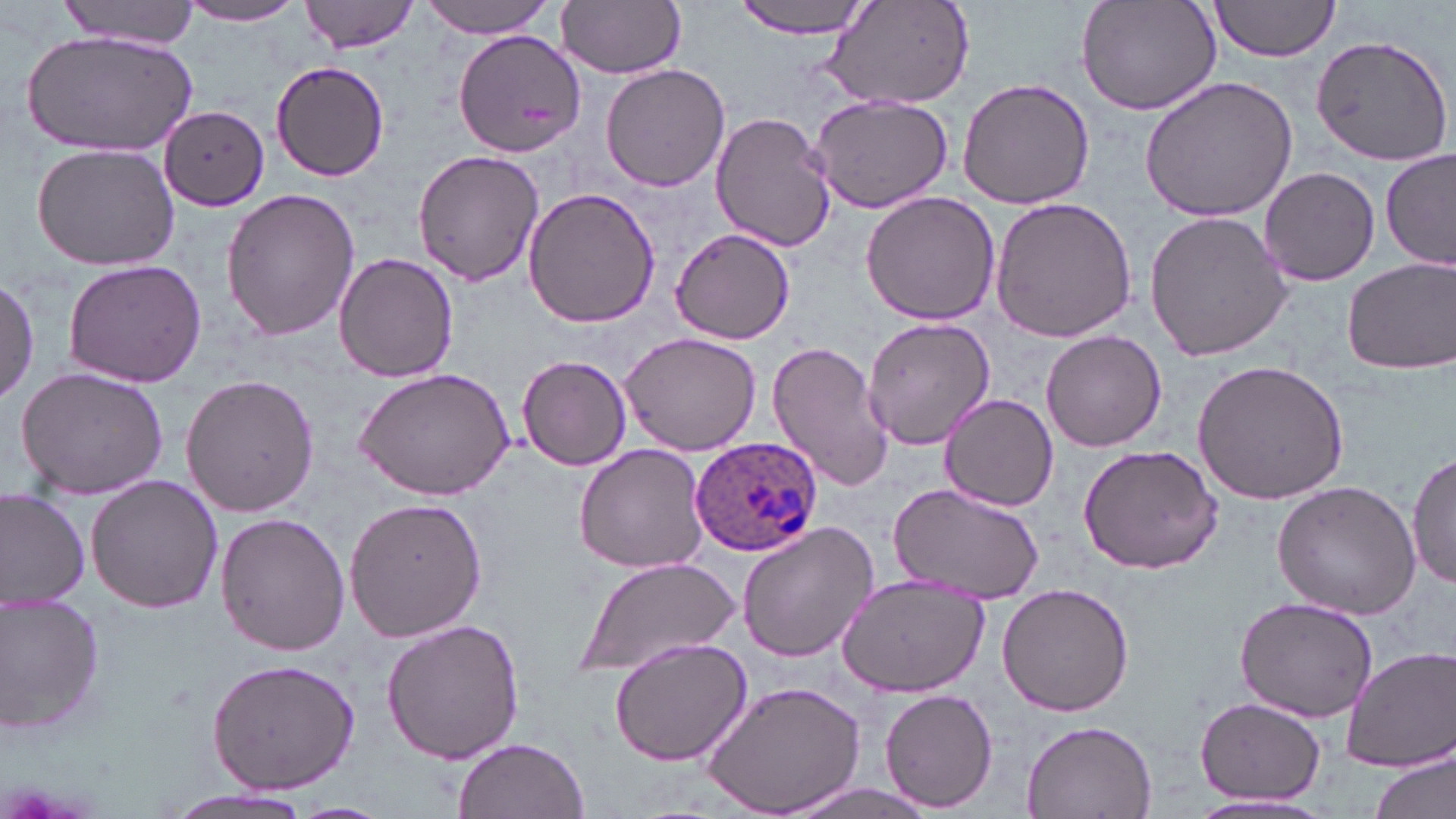

Approximate bounding boxes as (x1, y1, x2, y2) in pixels. Plasmodium ovale-infected red blood cell locations: (689, 434, 822, 558). Uninfected red blood cell locations: (58, 0, 202, 49), (301, 0, 421, 54), (422, 0, 560, 37), (558, 0, 686, 78), (732, 0, 880, 39), (1073, 0, 1224, 117), (1205, 0, 1342, 62), (177, 2, 309, 25), (820, 2, 976, 112), (452, 25, 588, 156), (23, 30, 195, 157), (1313, 33, 1452, 173), (271, 60, 392, 182), (601, 63, 731, 192), (956, 76, 1096, 210), (1138, 76, 1297, 223), (808, 93, 957, 214), (161, 107, 272, 210), (711, 112, 837, 253), (29, 141, 181, 272), (1381, 146, 1454, 275), (412, 150, 546, 286), (1258, 167, 1380, 285), (521, 184, 662, 330), (222, 188, 362, 342), (859, 190, 1002, 326), (989, 195, 1138, 345), (1144, 211, 1292, 363), (668, 227, 797, 345), (334, 251, 458, 383), (1342, 256, 1455, 375), (63, 259, 205, 389), (0, 275, 40, 406), (862, 315, 997, 451), (1040, 330, 1167, 452), (619, 333, 762, 458), (766, 342, 893, 492), (517, 354, 632, 471), (1191, 359, 1350, 505), (14, 367, 170, 500), (355, 367, 516, 502), (179, 375, 318, 517), (939, 393, 1061, 511), (573, 443, 710, 574), (1078, 444, 1224, 574), (1408, 448, 1455, 594), (86, 474, 224, 614), (1271, 480, 1422, 620), (884, 483, 1046, 604), (0, 487, 91, 608), (343, 496, 486, 643), (216, 512, 353, 657), (735, 519, 881, 663), (575, 557, 739, 681), (836, 575, 990, 698), (996, 584, 1135, 717), (1233, 594, 1379, 721), (1, 596, 106, 738), (383, 617, 524, 766), (608, 636, 753, 767), (1342, 647, 1456, 772), (206, 657, 361, 795), (702, 683, 867, 817), (881, 687, 998, 812), (1196, 696, 1326, 804), (1019, 721, 1157, 817), (453, 737, 587, 819), (1371, 748, 1455, 819), (782, 781, 939, 819), (158, 787, 319, 818), (1185, 795, 1338, 816), (287, 801, 393, 819). Slide-level diagnosis: Plasmodium ovale. May-Grünwald-Giemsa stain. Image is 1456×819 pixels. Light microscopy. Captured at 1000x magnification. Thin blood film. Single field of view.